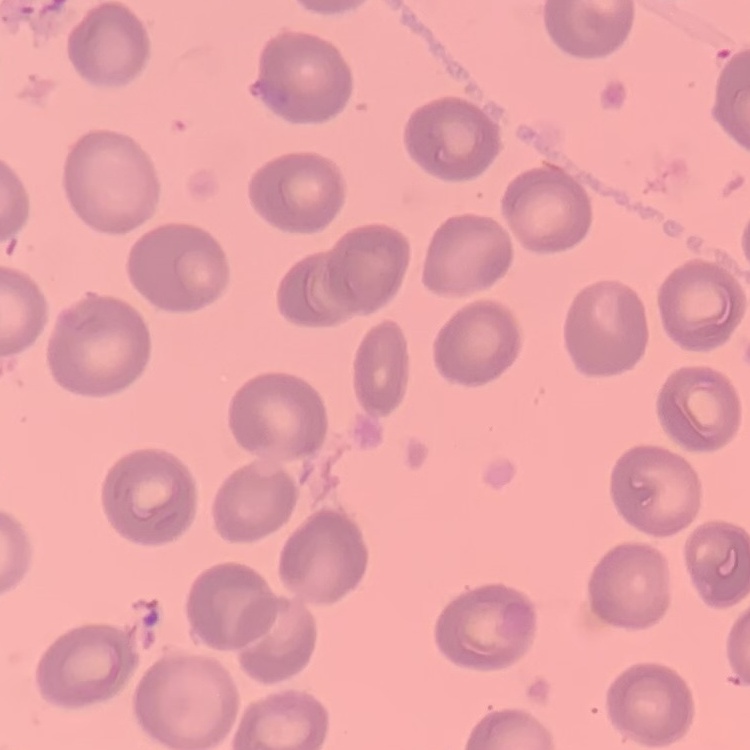

Summary:
  - Erythrocyte morphology: no rouleaux formation
  - Preparation: thin blood film
  - Image type: square crop of a larger photomicrograph
  - Stain: Field's or Giemsa